Give the position of every Plasmodium parasite, noting whether each is a trophozoite, schizont, or gametocyte.
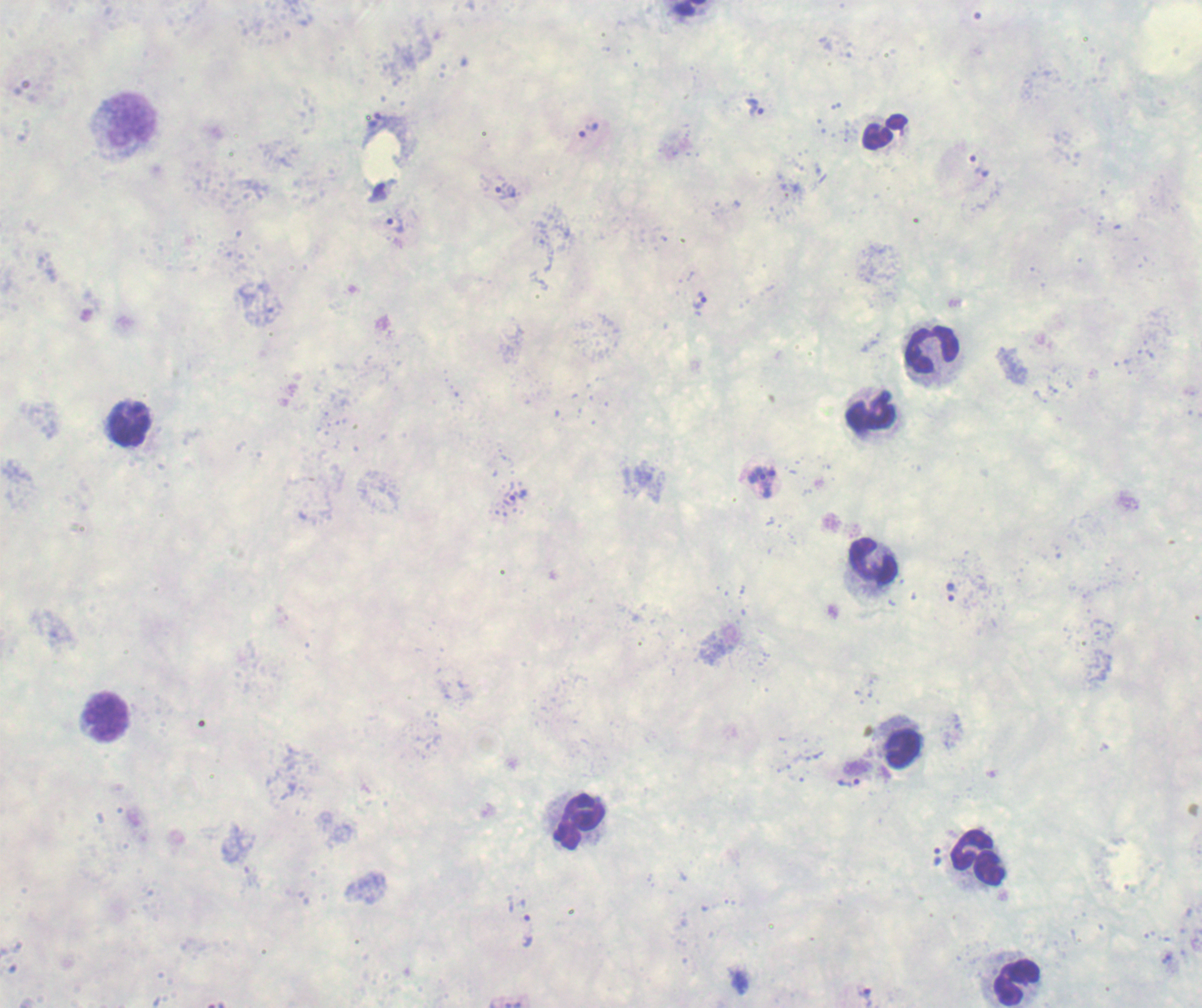
Approximate centers as (x, y) in pixels.
Trophozoites: (754, 108), (587, 130), (505, 192), (395, 225), (700, 302), (761, 483), (509, 498), (949, 591), (849, 782), (937, 856), (527, 931), (865, 995).
No schizont or gametocyte forms observed.

coordinate format = approximate centers as (x, y) in pixels
leukocyte locations = (126, 127), (883, 131), (932, 350), (871, 411), (126, 424), (874, 561), (103, 716), (899, 744), (578, 822), (979, 857), (1016, 982)
image size = 1202×1008 pixels
field of view = single
stain = Romanowsky
context = previously used in a real diagnosis
background quality = unsatisfactory
magnification = 100x
preparation = thick blood smear